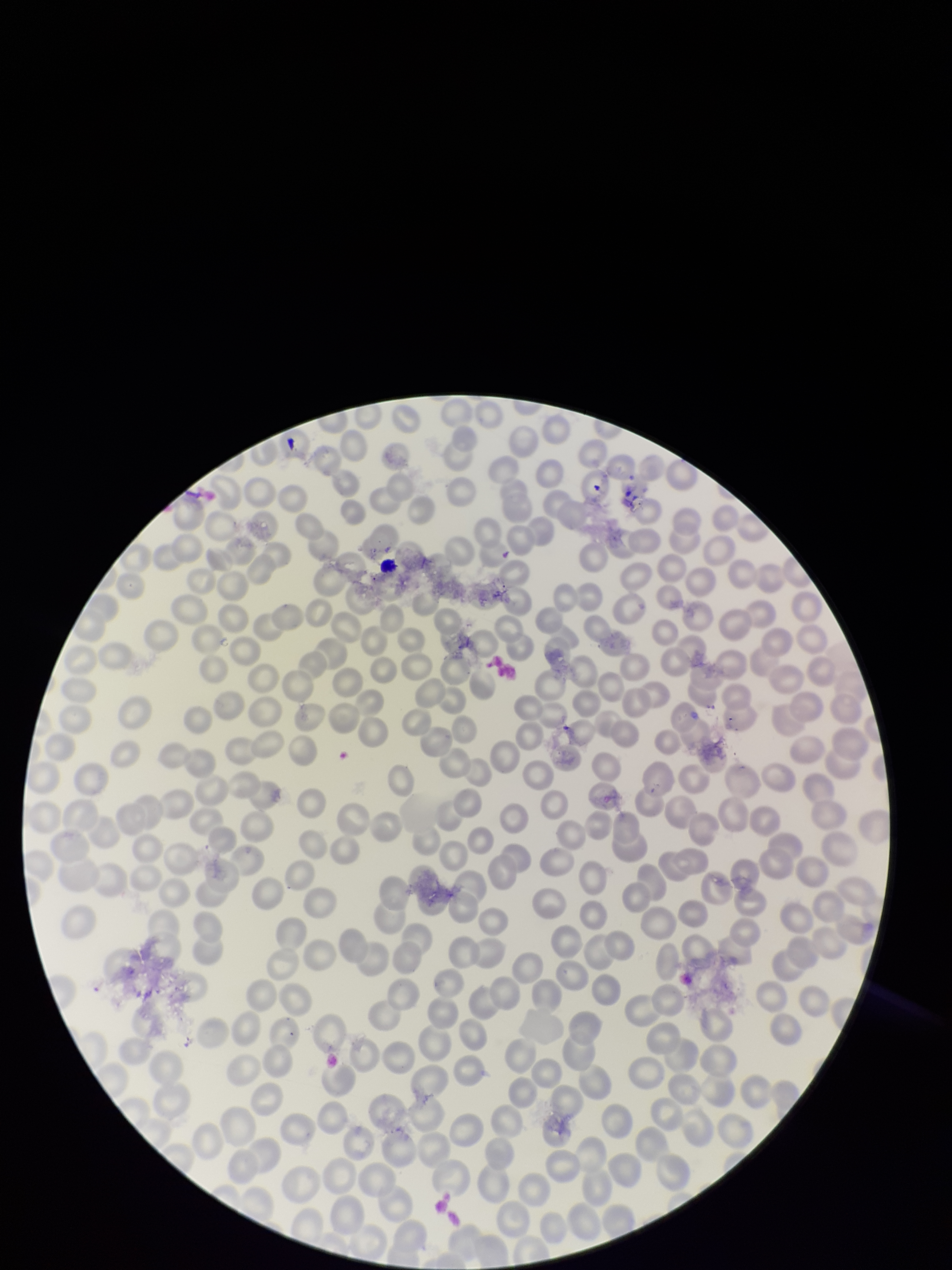 Red blood cell count: 270. Parasitized red blood cells: none identified. Species reported for this patient: Plasmodium falciparum. Preparation: thin. Stained with Giemsa. Parasitized red blood cell count: 0. Photographed through the microscope eyepiece with a smartphone camera. Single field of view. Image is 952×1270 pixels. Patient malaria status: infected.